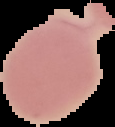
{
  "image_type": "segmented cell region on a black background",
  "image_size": "115×127 pixels",
  "malaria_status": "uninfected",
  "preparation": "thin blood smear"
}